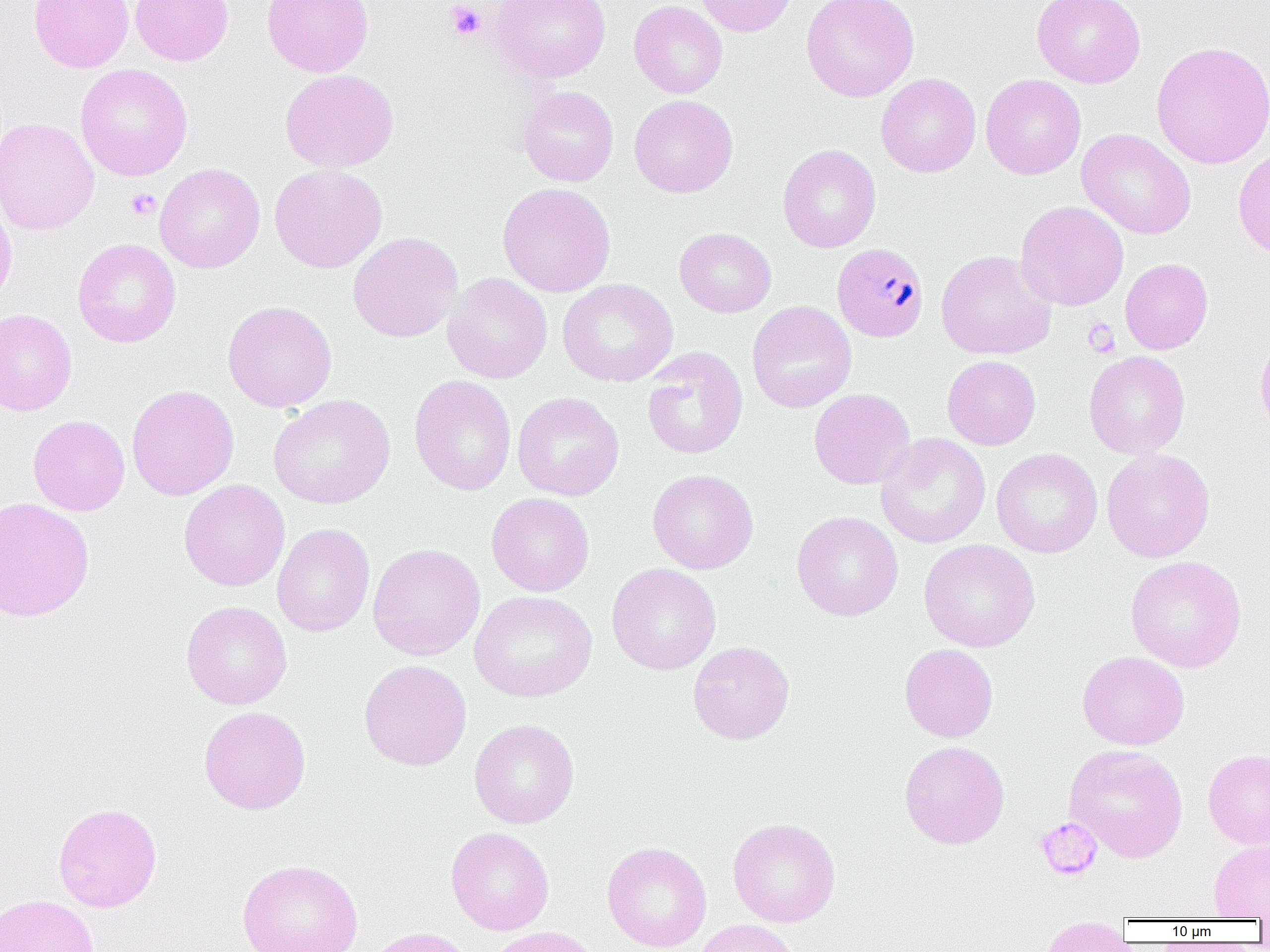
Summary:
  - Coordinate format: approximate bounding boxes as (x1, y1, x2, y2) in pixels
  - Uninfected red blood cell locations: (29, 0, 134, 72), (131, 0, 233, 65), (262, 0, 373, 77), (491, 0, 611, 82), (695, 0, 798, 37), (800, 0, 920, 102), (1032, 0, 1146, 88), (629, 1, 728, 99), (1151, 41, 1270, 169), (75, 64, 192, 180), (279, 68, 399, 172), (876, 73, 981, 177), (980, 74, 1086, 180), (517, 86, 618, 186), (629, 95, 738, 198), (0, 117, 99, 236), (1076, 128, 1197, 240), (777, 145, 881, 253), (1233, 148, 1270, 258), (154, 163, 265, 273), (269, 164, 388, 274), (497, 182, 616, 297), (0, 190, 17, 310), (1015, 200, 1129, 311), (674, 227, 777, 317), (347, 231, 463, 343), (72, 238, 181, 347), (935, 250, 1056, 360), (1120, 258, 1213, 354), (441, 273, 552, 384), (558, 279, 678, 387), (222, 300, 337, 412), (747, 301, 857, 413), (0, 309, 76, 416), (1255, 330, 1270, 440), (641, 347, 748, 460), (1083, 351, 1190, 459), (942, 355, 1041, 450), (409, 375, 516, 496), (126, 384, 239, 501), (808, 388, 915, 489), (512, 391, 624, 501), (268, 394, 396, 509), (28, 414, 130, 516), (876, 433, 990, 548), (991, 448, 1103, 558), (1101, 449, 1215, 563), (646, 469, 758, 575), (178, 479, 290, 591), (486, 492, 595, 597), (0, 497, 95, 621), (792, 511, 903, 621), (272, 523, 375, 637), (918, 539, 1040, 652), (367, 543, 485, 660), (1125, 555, 1247, 672), (607, 563, 721, 675), (469, 590, 597, 701), (181, 600, 292, 710), (688, 641, 795, 744), (899, 643, 998, 743), (1077, 650, 1190, 750), (358, 659, 472, 771), (198, 706, 311, 815), (469, 719, 580, 829), (899, 740, 1010, 849), (1064, 743, 1188, 863), (1203, 749, 1270, 848), (53, 802, 162, 912), (727, 818, 841, 927), (446, 827, 554, 935), (1208, 839, 1270, 920), (602, 841, 712, 952), (237, 859, 364, 952), (0, 894, 100, 952), (1040, 917, 1132, 952), (692, 919, 802, 952), (363, 926, 477, 952), (486, 926, 608, 952)
  - Plasmodium malariae-infected red blood cell locations: (832, 242, 929, 342)
  - Platelet locations: (446, 2, 485, 41), (125, 188, 160, 220), (1083, 318, 1121, 357), (1034, 818, 1102, 880)
  - Slide-level diagnosis: Plasmodium malariae
  - Field of view: one of a larger specimen
  - Preparation: thin blood smear
  - Image size: 1270×952 pixels
  - Magnification: 1000x
  - Modality: light microscopy